State the blood parasite species.
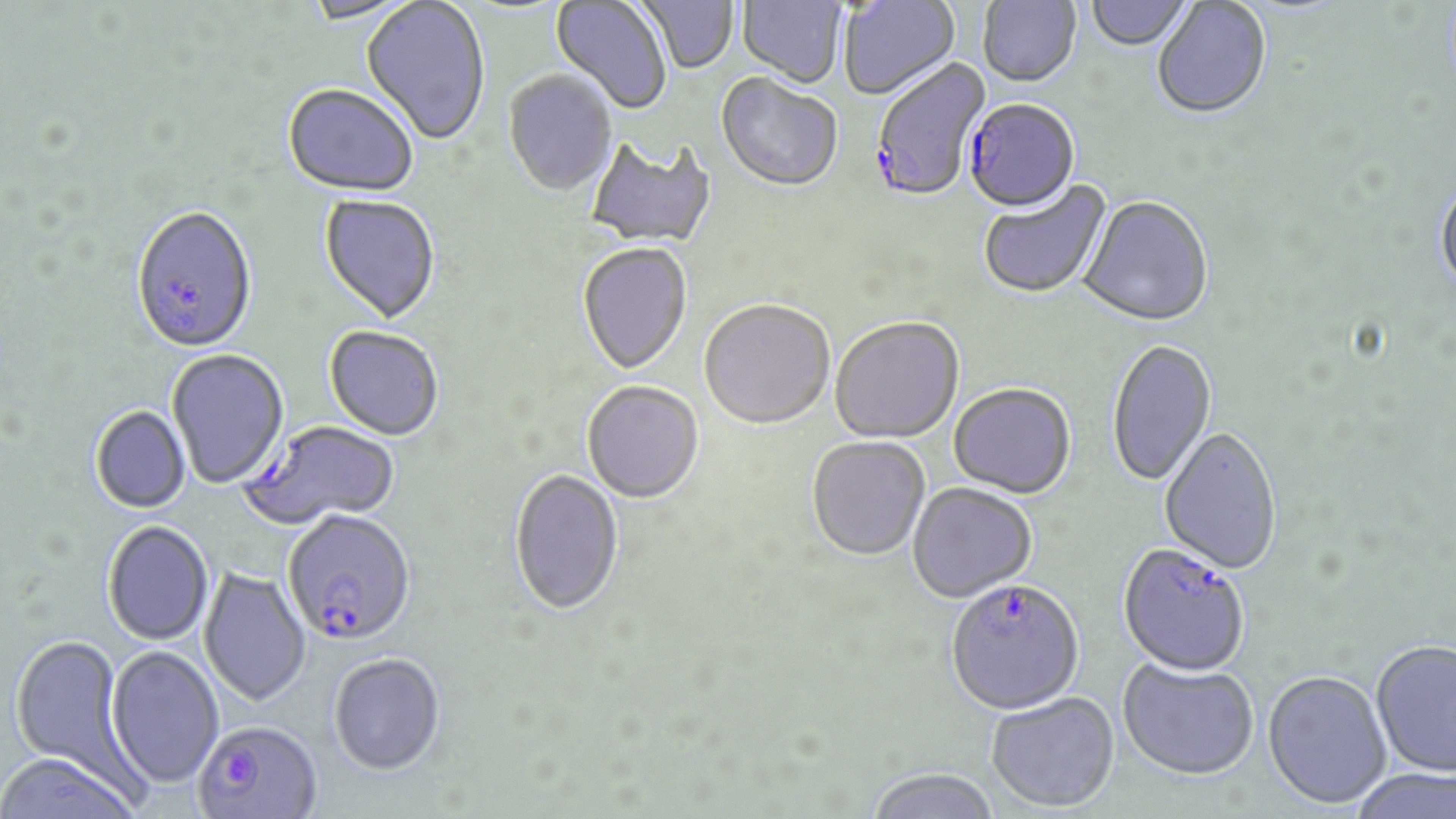
Plasmodium falciparum.

{
  "stain": "May-Grünwald-Giemsa",
  "modality": "light microscopy",
  "magnification": "1000x",
  "preparation": "thin blood film",
  "image_size": "1456×819 pixels",
  "uninfected_red_blood_cell_locations": "approximate bounding boxes as (x1, y1, x2, y2) in pixels: (361, 0, 490, 148), (551, 0, 672, 116), (637, 0, 738, 75), (736, 0, 847, 89), (839, 0, 959, 102), (977, 0, 1081, 89), (1086, 0, 1194, 53), (299, 1, 419, 27), (1152, 1, 1272, 122), (503, 70, 618, 198), (716, 74, 843, 194), (282, 86, 419, 199), (585, 135, 717, 248), (1435, 180, 1456, 296), (978, 181, 1112, 301), (319, 195, 441, 326), (1078, 197, 1214, 328), (577, 242, 693, 376), (698, 301, 835, 432), (830, 318, 964, 444), (324, 327, 443, 442), (1106, 339, 1217, 488), (167, 349, 289, 489), (582, 383, 704, 505), (948, 384, 1076, 499), (90, 406, 191, 514), (1159, 426, 1282, 574), (807, 437, 930, 562), (509, 469, 623, 618), (907, 482, 1037, 603), (102, 521, 213, 646), (198, 566, 311, 708), (9, 634, 135, 784), (1370, 639, 1456, 778), (106, 646, 224, 789), (329, 653, 445, 776), (1118, 657, 1259, 779), (1263, 668, 1392, 808), (986, 691, 1119, 811), (0, 754, 143, 818), (865, 767, 1001, 819), (1347, 768, 1456, 819)",
  "plasmodium_falciparum_infected_red_blood_cell_locations": "approximate bounding boxes as (x1, y1, x2, y2) in pixels: (871, 57, 991, 204), (968, 97, 1081, 210), (130, 207, 258, 356), (248, 422, 399, 527), (282, 512, 416, 648), (1118, 541, 1251, 675), (944, 577, 1084, 714), (194, 721, 322, 819)",
  "field_of_view": "single"
}